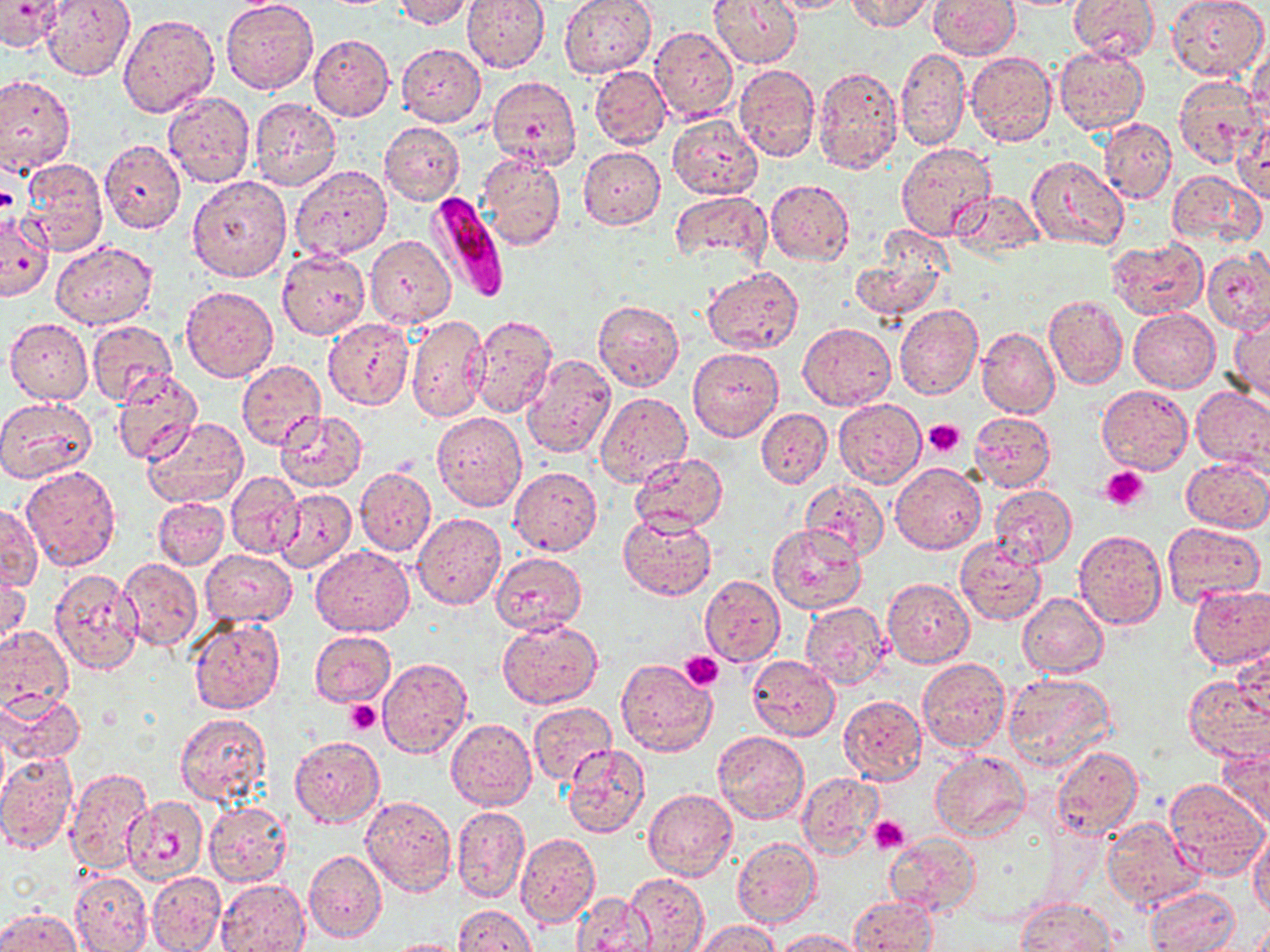 Approximate bounding boxes as (x1, y1, x2, y2) in pixels. Platelet locations: (0, 185, 20, 214), (923, 418, 965, 457), (1100, 465, 1150, 511), (681, 651, 724, 692), (344, 699, 382, 734), (869, 816, 910, 851). Uninfected red blood cell locations: (41, 0, 135, 82), (221, 0, 319, 95), (391, 0, 474, 28), (461, 0, 549, 72), (559, 0, 658, 79), (709, 0, 803, 70), (765, 0, 859, 14), (846, 0, 936, 32), (928, 0, 1020, 59), (1069, 0, 1161, 65), (1166, 0, 1268, 81), (0, 3, 67, 53), (117, 14, 219, 118), (649, 26, 738, 122), (309, 35, 394, 120), (1248, 35, 1269, 125), (396, 42, 485, 127), (1053, 47, 1149, 134), (896, 48, 970, 149), (597, 51, 721, 139), (966, 52, 1057, 148), (734, 64, 820, 162), (813, 64, 904, 176), (590, 67, 671, 148), (0, 74, 75, 173), (1173, 75, 1266, 169), (487, 76, 582, 171), (163, 91, 255, 189), (249, 98, 341, 190), (667, 116, 762, 200), (1235, 116, 1269, 204), (1101, 118, 1176, 204), (379, 121, 464, 206), (99, 139, 186, 234), (896, 142, 996, 242), (578, 146, 666, 229), (476, 152, 566, 250), (1026, 155, 1129, 251), (20, 158, 109, 257), (290, 164, 392, 259), (1168, 170, 1263, 247), (187, 174, 292, 282), (765, 179, 854, 265), (668, 191, 773, 274), (950, 191, 1045, 257), (1, 211, 55, 302), (365, 235, 454, 327), (1105, 237, 1207, 321), (851, 238, 951, 324), (50, 241, 157, 327), (1202, 249, 1270, 333), (277, 250, 370, 340), (702, 265, 804, 354), (181, 284, 278, 382), (1044, 293, 1128, 390), (594, 300, 684, 392), (894, 304, 984, 401), (1128, 307, 1219, 391), (1229, 309, 1269, 404), (405, 314, 490, 422), (470, 314, 558, 419), (6, 318, 93, 404), (87, 319, 176, 406), (323, 319, 413, 410), (798, 322, 894, 410), (977, 326, 1060, 418), (486, 327, 601, 440), (687, 347, 783, 441), (520, 354, 615, 460), (237, 360, 325, 448), (110, 370, 201, 464), (1098, 386, 1193, 473), (1192, 387, 1270, 474), (595, 391, 691, 486), (0, 396, 98, 483), (833, 399, 926, 487), (755, 406, 832, 489), (275, 410, 368, 493), (968, 410, 1056, 494), (433, 412, 526, 511), (142, 418, 249, 509), (238, 447, 349, 564), (629, 452, 727, 533), (1181, 457, 1269, 532), (890, 462, 985, 553), (21, 465, 121, 571), (355, 467, 436, 557), (509, 467, 602, 555), (226, 472, 304, 558), (801, 480, 888, 561), (989, 484, 1078, 569), (275, 487, 357, 572), (153, 497, 229, 570), (0, 503, 41, 591), (619, 510, 717, 600), (412, 513, 505, 609), (1163, 523, 1263, 604), (767, 525, 866, 614), (1073, 530, 1167, 628), (955, 537, 1049, 627), (310, 545, 413, 636), (201, 548, 296, 627), (490, 551, 586, 636), (118, 558, 202, 651), (1, 565, 31, 653), (49, 569, 144, 676), (701, 575, 784, 666), (882, 579, 974, 668), (1186, 586, 1270, 670), (1018, 592, 1108, 677), (800, 601, 891, 691), (188, 617, 286, 714), (497, 621, 602, 707), (0, 627, 73, 709), (309, 630, 396, 707), (1231, 646, 1268, 722), (748, 656, 839, 740), (378, 657, 472, 758), (918, 658, 1010, 753), (615, 659, 718, 758), (1003, 672, 1115, 773), (1182, 676, 1270, 763), (0, 691, 85, 764), (839, 694, 927, 784), (528, 701, 616, 785), (174, 712, 273, 804), (531, 715, 637, 829), (446, 718, 537, 811), (712, 731, 809, 824), (290, 736, 383, 827), (1217, 741, 1270, 828), (562, 744, 652, 840), (1052, 746, 1144, 840), (0, 752, 78, 854), (930, 753, 1029, 841), (65, 768, 153, 874), (797, 771, 884, 861), (1163, 778, 1268, 881), (643, 788, 737, 880), (361, 795, 456, 897), (123, 796, 208, 884), (203, 801, 293, 889), (451, 805, 530, 903), (1101, 816, 1205, 911), (1248, 826, 1270, 919), (515, 832, 601, 928), (886, 833, 980, 917), (732, 836, 821, 929), (303, 849, 386, 943), (624, 870, 709, 952), (70, 871, 152, 952), (146, 871, 226, 952), (216, 879, 311, 952), (1146, 887, 1239, 952), (572, 893, 655, 951), (849, 895, 937, 951), (1015, 897, 1119, 952), (453, 905, 537, 952), (0, 907, 81, 952), (693, 920, 781, 952), (773, 929, 865, 951), (384, 938, 469, 952). Plasmodium falciparum-infected red blood cell locations: (426, 191, 508, 300). Slide-level diagnosis: Plasmodium falciparum. Captured at 1000x magnification. Optical microscopy. May-Grünwald-Giemsa stain. Image is 1270×952 pixels. Thin blood smear. Single field of view.